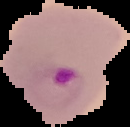
image size = 130×127 pixels
image type = segmented cell region with the area outside set to black
malaria status = parasitized
preparation = thin blood smear